Report the malaria status of this cell.
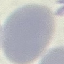
Uninfected.

Acquired by smartphone through the microscope eyepiece. Giemsa-stained preparation. Cell patch, automatically extracted from a larger field of view and resized to 64 × 64 pixels. Thin blood film.